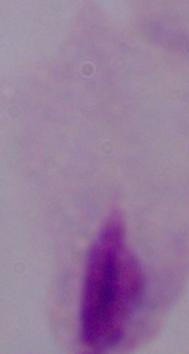
A trichomonad is shown. Micrograph. 1000x magnification.